Locate platelets.
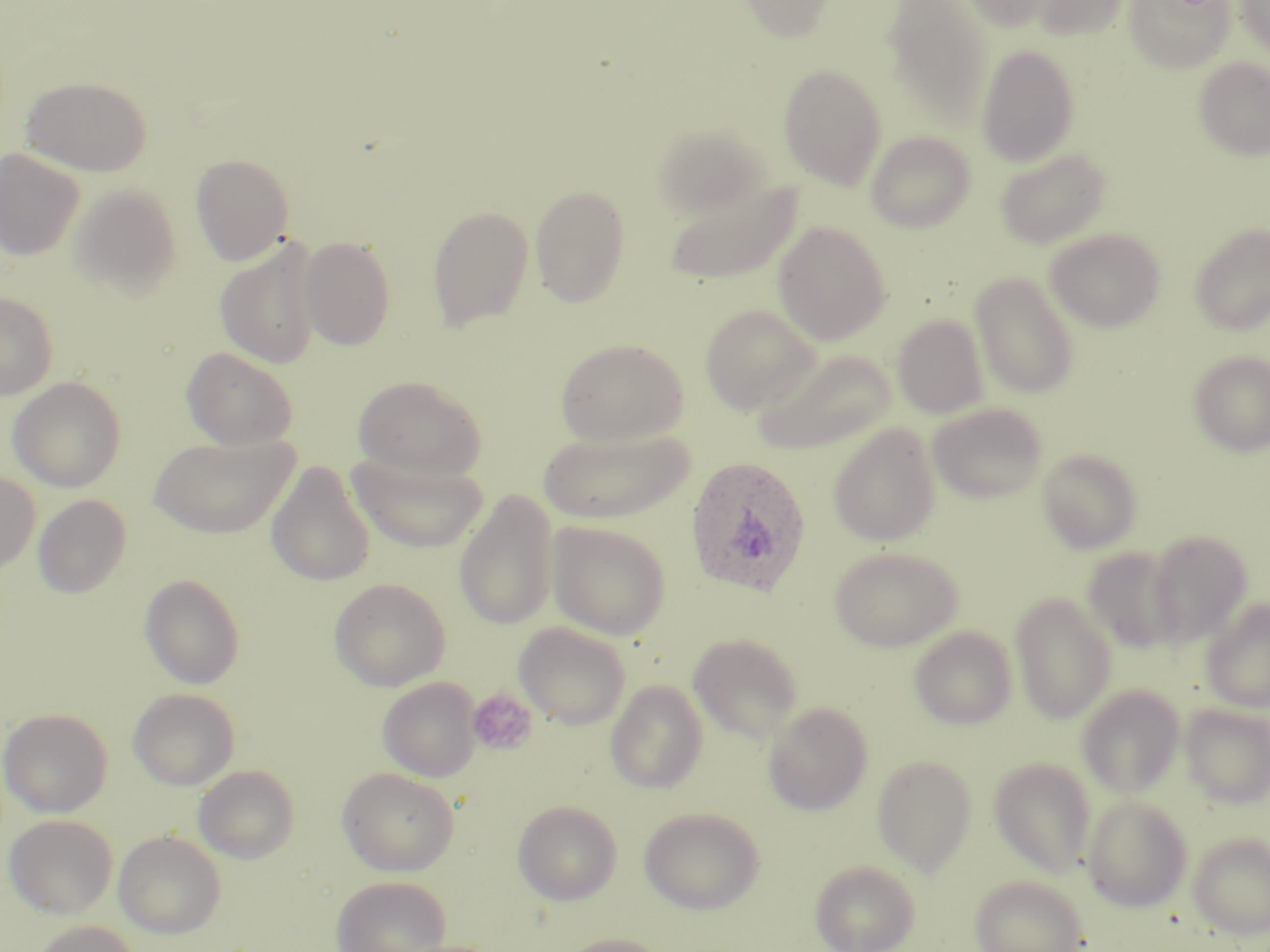

Approximate bounding boxes as (x1,y1)-(x2,y2) corner pairs in pixels.
Platelets: (467,688)-(538,756).

Summary:
  - Uninfected red blood cell locations: (739,0)-(835,41), (882,0)-(995,129), (959,0)-(1058,31), (1028,0)-(1129,41), (1124,0)-(1234,74), (1236,0)-(1270,58), (976,45)-(1080,167), (1194,57)-(1270,161), (778,64)-(887,190), (20,75)-(152,176), (652,122)-(770,219), (866,130)-(976,234), (0,148)-(85,261), (995,148)-(1112,250), (191,153)-(295,265), (661,176)-(803,285), (68,184)-(182,298), (530,185)-(630,308), (427,205)-(534,331), (773,221)-(891,345), (1189,223)-(1270,335), (1045,228)-(1165,333), (298,236)-(396,350), (215,240)-(323,369), (970,271)-(1079,399), (0,291)-(58,400), (700,304)-(821,415), (893,315)-(989,419), (555,338)-(689,446), (182,347)-(298,450), (754,348)-(897,456), (1188,350)-(1270,457), (8,376)-(127,492), (352,376)-(487,481), (927,402)-(1048,504), (827,422)-(942,547), (539,427)-(695,524), (147,434)-(298,538), (1036,448)-(1142,554), (346,452)-(488,553), (266,461)-(376,587), (0,471)-(41,572), (454,490)-(559,632), (33,494)-(131,598), (547,521)-(672,640), (1147,530)-(1253,646), (829,545)-(964,652), (1080,547)-(1183,654), (139,573)-(245,689), (329,578)-(450,691), (1010,592)-(1117,724), (1200,597)-(1270,713), (514,622)-(632,729), (909,625)-(1017,729), (688,632)-(804,744), (377,678)-(480,782), (605,679)-(708,793), (1076,683)-(1185,798), (128,688)-(240,790), (763,701)-(873,815), (1180,703)-(1270,808), (0,708)-(112,817), (872,754)-(977,876), (988,757)-(1096,878), (193,764)-(300,864), (337,767)-(461,876), (1082,794)-(1193,912), (513,800)-(622,905), (639,806)-(765,913), (3,814)-(118,918), (113,829)-(227,939), (1186,831)-(1270,939), (809,859)-(920,952), (968,874)-(1089,952), (332,875)-(452,952), (31,920)-(141,952), (554,933)-(675,952)
  - Plasmodium ovale-infected red blood cell locations: (684,455)-(812,598)
  - Slide-level diagnosis: Plasmodium ovale
  - Stain: May-Grünwald-Giemsa
  - Image size: 1270×952 pixels
  - Modality: optical microscopy
  - Field of view: single
  - Preparation: thin blood film
  - Magnification: 1000x